Give the preparation type.
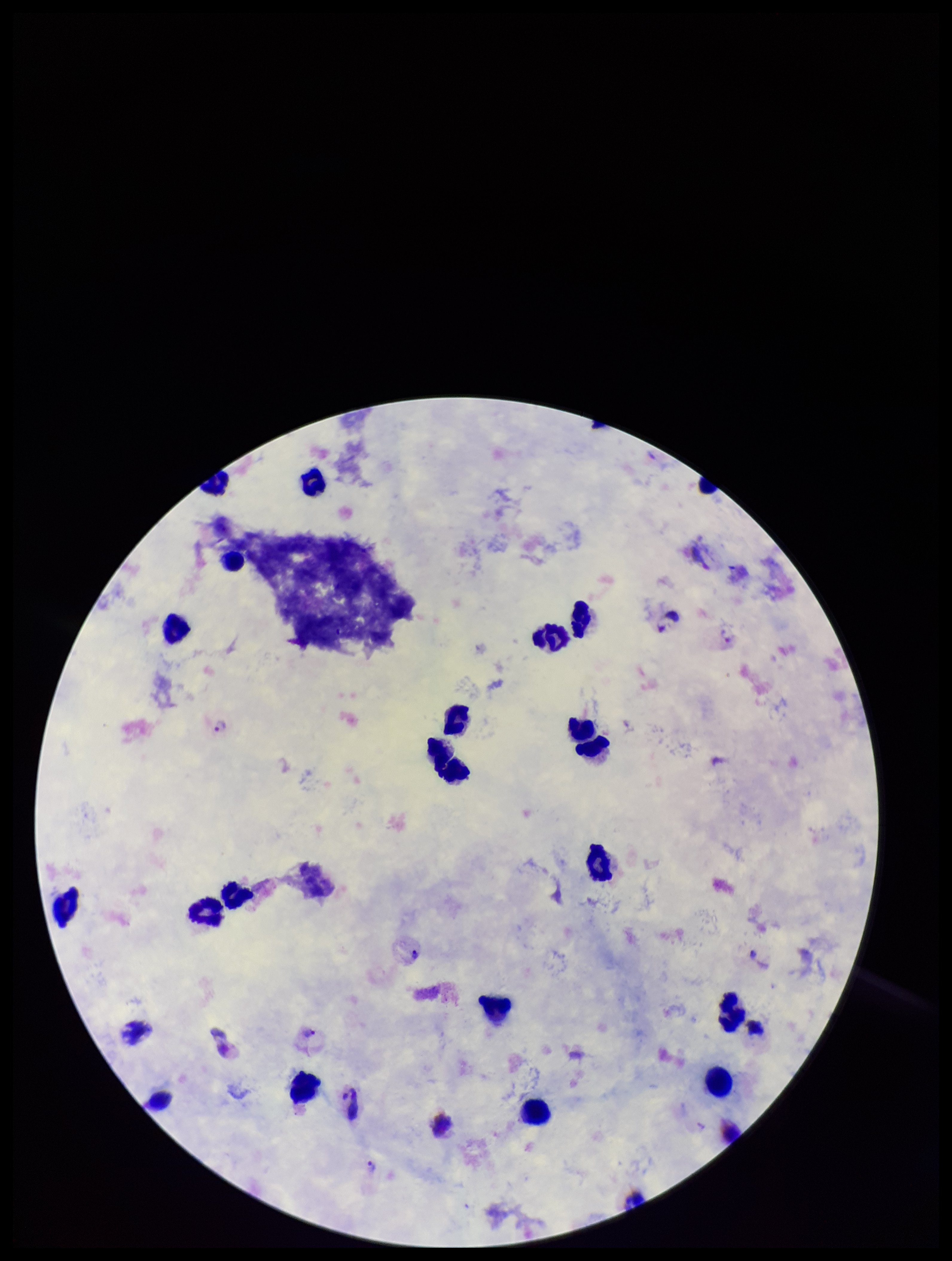
Thick.

Summary:
  - Parasite count: 3
  - Species reported for this patient: Plasmodium vivax
  - Stain: Giemsa
  - Leukocyte count: 20
  - Field of view: single
  - Capture: smartphone photograph through the microscope eyepiece
  - Patient malaria status: positive
  - Image size: 952×1261 pixels
  - Plasmodium parasites: seen